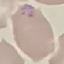

result = malaria parasites identified
capture = smartphone through the microscope eyepiece
stain = Giemsa
image type = automatically extracted cell patch, resized to 64 × 64 pixels
preparation = thin blood film